Identify the blood parasite species.
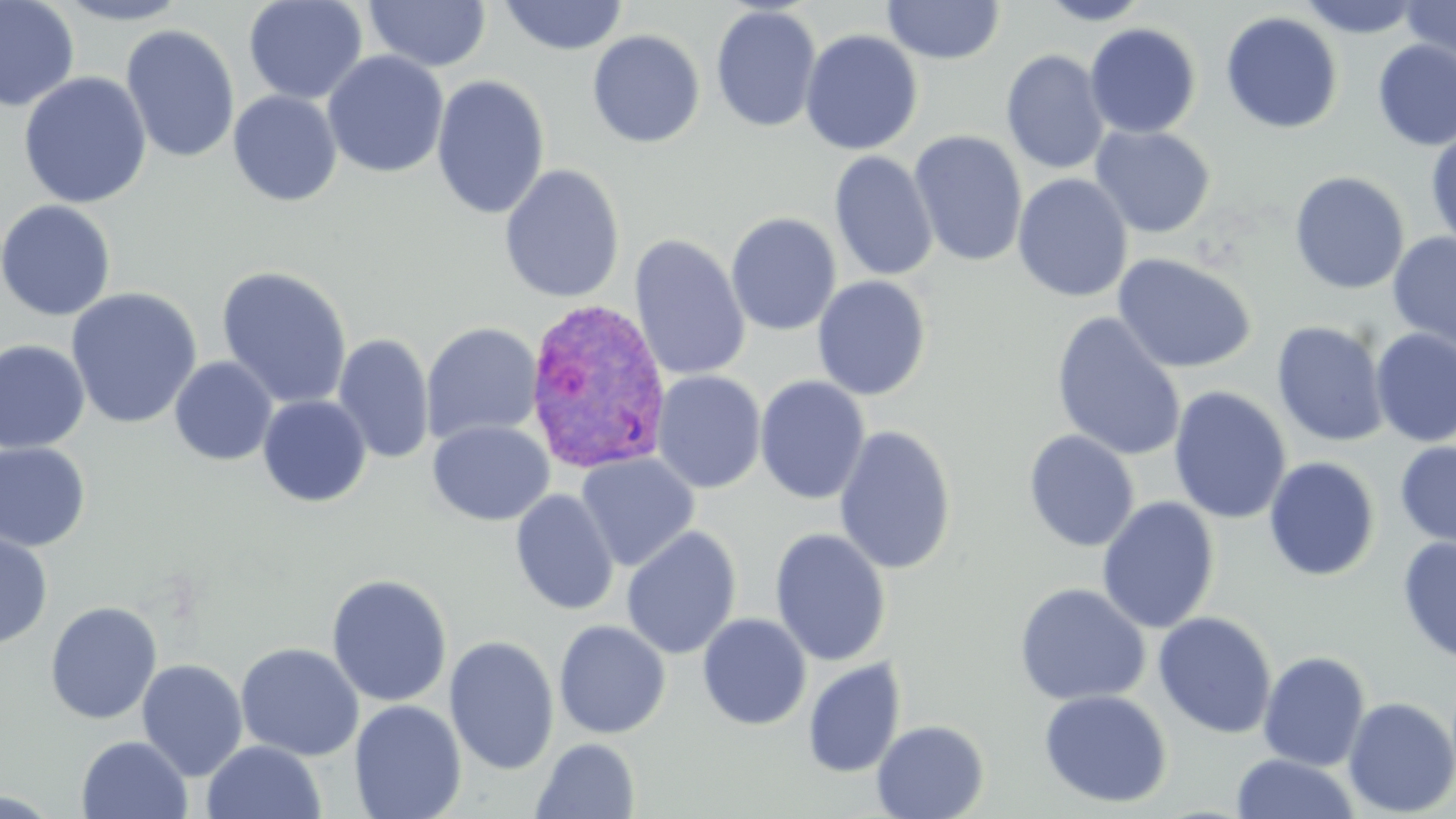

Plasmodium vivax.

image size = 1456×819 pixels
uninfected red blood cell locations = approximate bounding boxes as [x1, y1, x2, y2] in pixels: [0, 0, 80, 112], [53, 0, 194, 25], [243, 0, 368, 104], [364, 0, 491, 72], [498, 0, 629, 57], [1035, 0, 1154, 25], [1297, 0, 1424, 38], [1398, 0, 1456, 70], [882, 1, 1005, 65], [710, 5, 823, 133], [1220, 11, 1343, 134], [1084, 23, 1201, 138], [120, 24, 241, 164], [587, 29, 705, 149], [800, 29, 923, 155], [1372, 40, 1456, 151], [1001, 49, 1110, 175], [322, 51, 449, 179], [17, 71, 153, 209], [431, 75, 551, 220], [227, 90, 343, 207], [1090, 125, 1216, 237], [1426, 126, 1456, 251], [909, 130, 1028, 268], [829, 150, 939, 282], [498, 164, 626, 304], [1289, 170, 1410, 295], [1012, 173, 1133, 303], [0, 200, 117, 322], [726, 212, 842, 336], [1387, 232, 1456, 358], [629, 233, 751, 382], [1113, 253, 1257, 374], [216, 265, 353, 411], [812, 276, 932, 400], [65, 287, 203, 429], [1050, 312, 1187, 462], [1271, 321, 1390, 448], [422, 322, 543, 445], [1370, 328, 1456, 448], [333, 333, 434, 465], [0, 339, 91, 454], [169, 356, 278, 466], [651, 370, 766, 494], [755, 376, 871, 505], [1168, 385, 1291, 525], [257, 395, 372, 507], [428, 420, 554, 526], [833, 424, 958, 576], [1022, 429, 1140, 552], [1394, 440, 1456, 552], [0, 442, 92, 553], [576, 453, 700, 572], [1263, 456, 1380, 582], [511, 489, 619, 616], [1097, 496, 1220, 634], [621, 525, 742, 660], [0, 528, 54, 650], [769, 528, 892, 666], [1397, 536, 1456, 665], [326, 573, 453, 708], [1014, 583, 1151, 706], [45, 601, 162, 724], [1153, 611, 1277, 739], [697, 613, 812, 730], [553, 620, 672, 739], [444, 636, 560, 776], [235, 642, 364, 760], [1258, 651, 1371, 772], [803, 658, 906, 778], [136, 659, 248, 781], [1038, 689, 1173, 808], [1342, 696, 1456, 817], [349, 700, 467, 819], [871, 719, 989, 819], [76, 735, 192, 819], [531, 737, 641, 818], [201, 740, 326, 819], [1230, 753, 1360, 818]
preparation = thin blood film
field of view = single
magnification = 1000x
stain = May-Grünwald-Giemsa
Plasmodium vivax-infected red blood cell locations = approximate bounding boxes as [x1, y1, x2, y2] in pixels: [523, 297, 672, 475]
modality = light microscopy